Assess this cell for malaria.
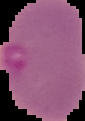
Parasitized.

{
  "image_type": "segmented cell region on a black background",
  "preparation": "thin blood smear",
  "image_size": "85×121 pixels"
}